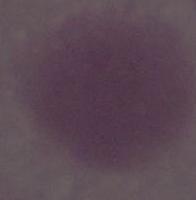
Summary:
  - Modality: micrograph
  - Magnification: 1000x
  - Identification: red blood cell